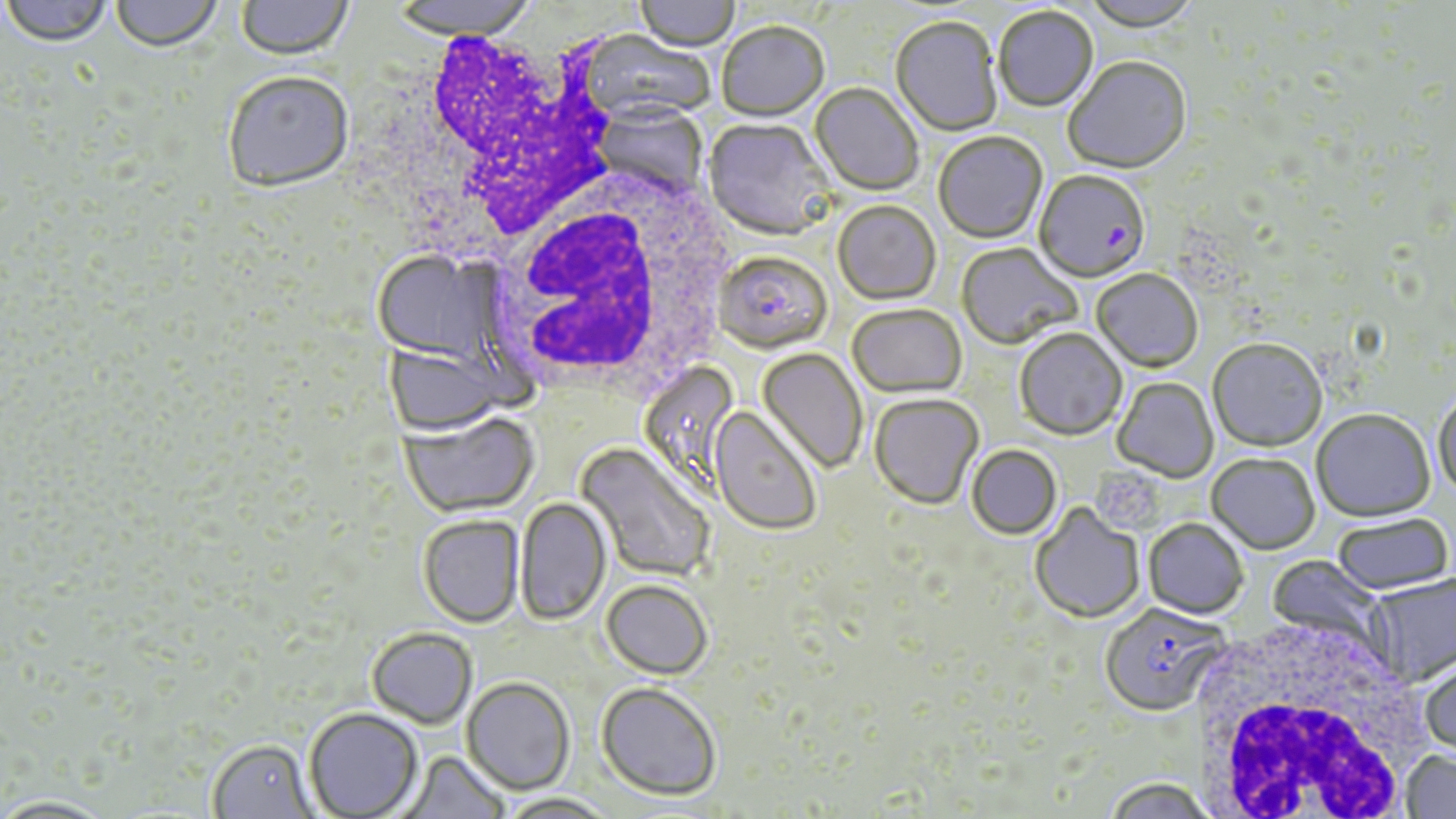
Summary:
  - Coordinate format: approximate bounding boxes as [x1, y1, x2, y2] in pixels
  - White blood cell locations: [392, 30, 626, 258], [483, 164, 738, 399], [1185, 622, 1425, 819]
  - Plasmodium falciparum-infected red blood cell locations: [1034, 172, 1151, 286], [714, 254, 832, 357], [1099, 606, 1228, 720]
  - Uninfected red blood cell locations: [0, 0, 114, 50], [110, 0, 224, 55], [236, 0, 354, 63], [389, 0, 540, 42], [635, 0, 740, 54], [1081, 0, 1203, 34], [993, 7, 1099, 113], [890, 18, 1002, 137], [716, 24, 829, 123], [576, 30, 714, 127], [1063, 57, 1192, 176], [223, 74, 354, 196], [809, 85, 923, 197], [596, 102, 707, 198], [703, 120, 835, 243], [934, 133, 1048, 245], [833, 202, 941, 306], [956, 244, 1082, 352], [372, 251, 488, 364], [1091, 270, 1203, 374], [847, 306, 967, 400], [1014, 330, 1128, 443], [1208, 342, 1327, 454], [383, 343, 507, 436], [757, 349, 868, 474], [639, 360, 741, 492], [1112, 378, 1219, 484], [1433, 391, 1456, 503], [869, 395, 984, 512], [710, 408, 821, 536], [1311, 411, 1435, 525], [398, 412, 539, 519], [575, 443, 714, 583], [967, 446, 1062, 541], [1207, 456, 1320, 556], [515, 497, 611, 627], [1030, 504, 1145, 625], [417, 516, 524, 629], [1333, 516, 1454, 596], [1143, 520, 1248, 621], [1266, 555, 1388, 651], [1368, 574, 1456, 689], [601, 580, 713, 680], [366, 628, 477, 729], [1419, 657, 1456, 762], [461, 678, 575, 796], [595, 682, 722, 801], [304, 708, 423, 819], [207, 739, 316, 818], [398, 750, 510, 818], [1400, 751, 1456, 819], [1103, 780, 1217, 819], [496, 793, 617, 819], [1, 795, 116, 818]
  - Slide-level diagnosis: Plasmodium falciparum
  - Modality: optical microscopy
  - Magnification: 1000x
  - Stain: May-Grünwald-Giemsa
  - Preparation: thin blood smear
  - Field of view: single
  - Image size: 1456×819 pixels